Report the malaria status of this cell.
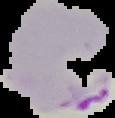
Parasitized.

Summary:
  - Image size: 115×118 pixels
  - Image type: cell region segmented out of the field of view; surrounding area masked to black
  - Preparation: thin blood film